Identify the parasite.
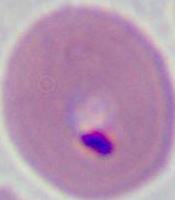

Plasmodium.

Summary:
  - Modality: micrograph
  - Magnification: 400x or 1000x